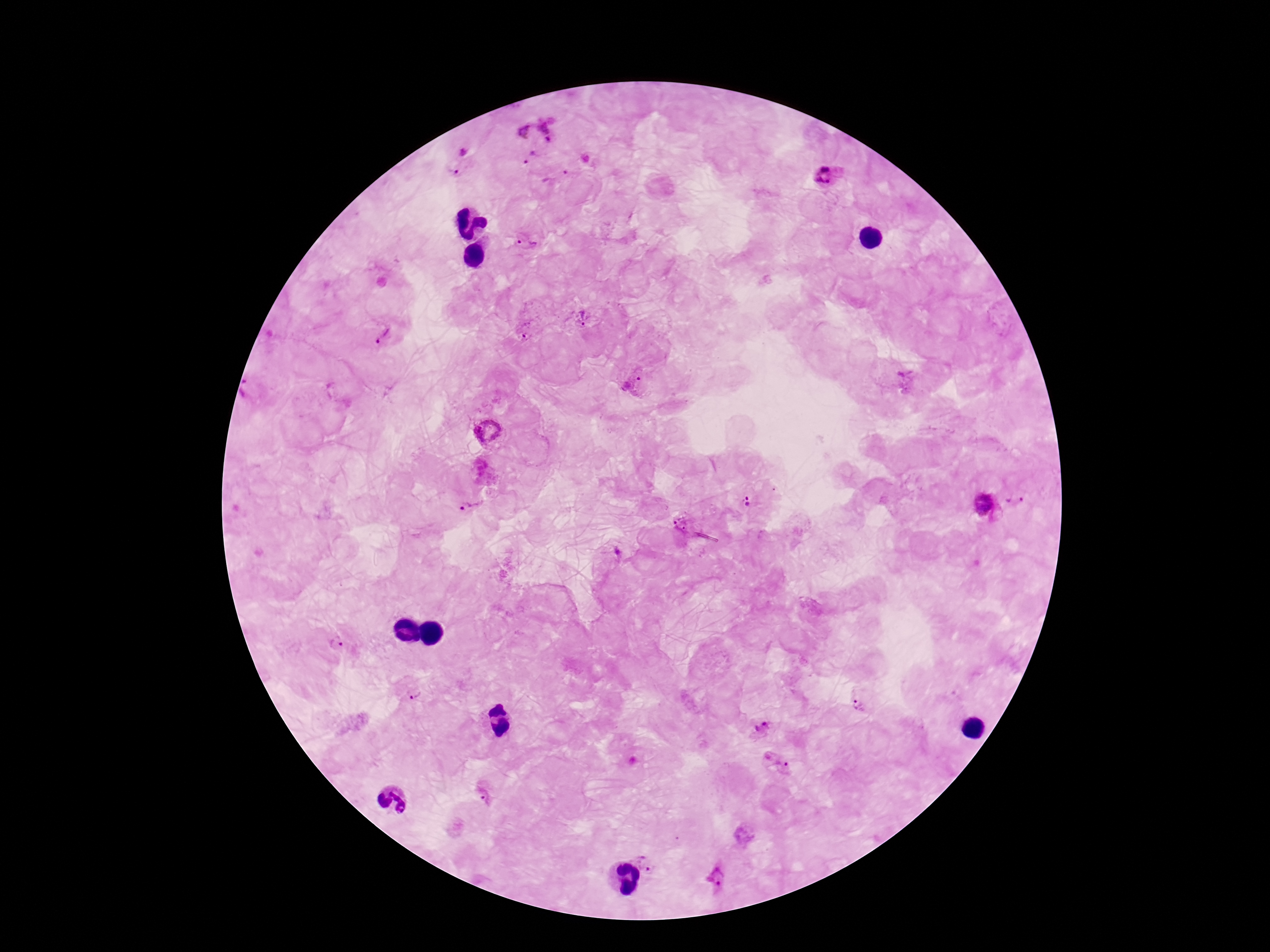

Approximate object centers, in pixels from the top-left corner.
Summary:
  - Plasmodium parasite locations: (x=552, y=125), (x=520, y=127), (x=528, y=156), (x=462, y=163), (x=555, y=176), (x=831, y=176), (x=527, y=244), (x=583, y=318), (x=525, y=330), (x=381, y=335), (x=910, y=379), (x=634, y=383), (x=253, y=395), (x=488, y=430), (x=747, y=500), (x=1015, y=501), (x=984, y=504), (x=469, y=507), (x=683, y=523), (x=617, y=554), (x=338, y=642), (x=414, y=691), (x=859, y=704), (x=760, y=728), (x=775, y=761), (x=482, y=794), (x=649, y=862), (x=719, y=878)
  - Capture: smartphone camera through the microscope eyepiece
  - Image size: 1270×952 pixels
  - Magnification: 100x
  - Patient malaria status: positive
  - Preparation: thick blood film
  - Stain: Giemsa
  - Field of view: one from this slide